Outline each Plasmodium ovale-infected red blood cell.
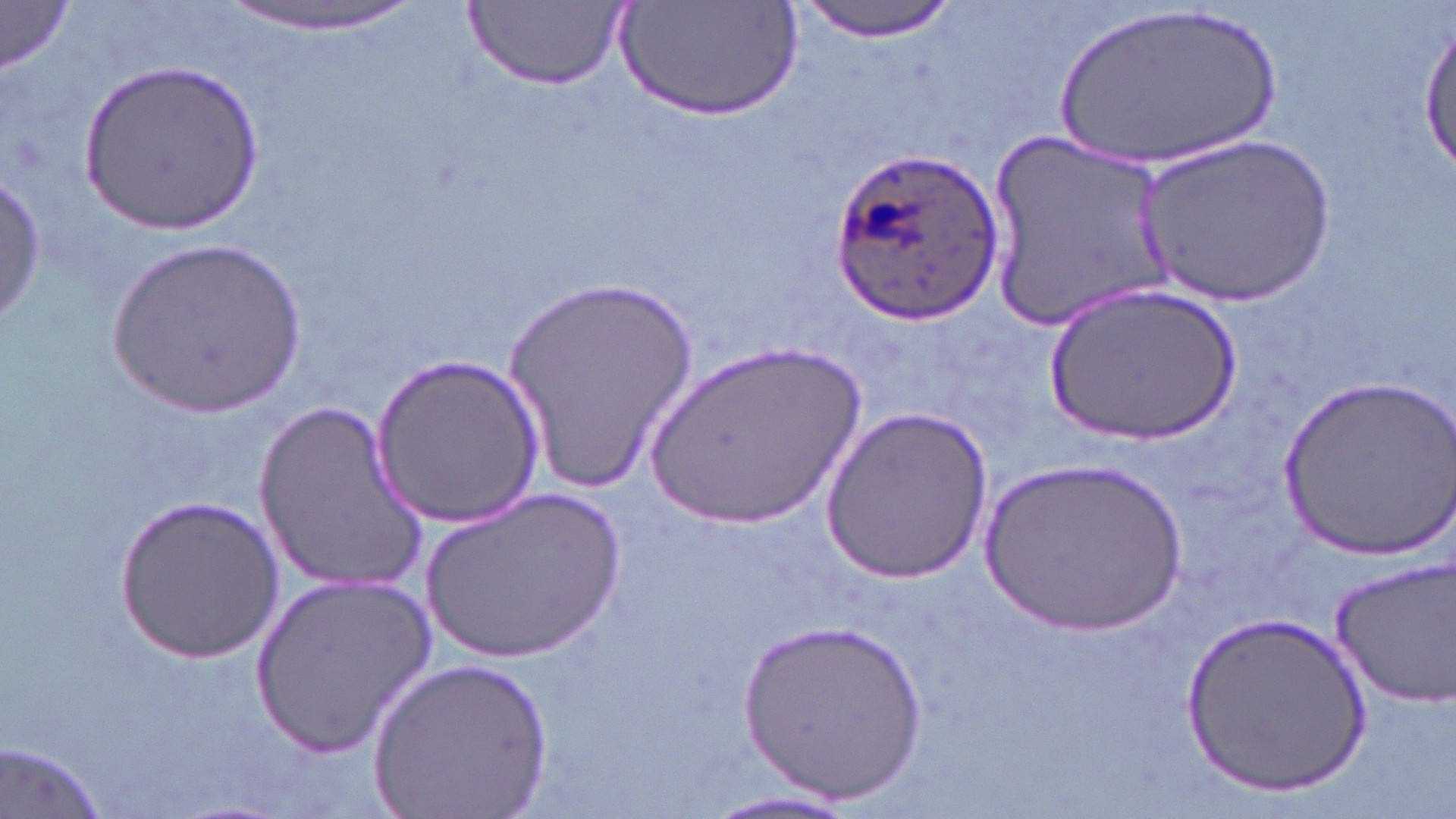

Approximate bounding boxes as (x1, y1, x2, y2) in pixels.
Plasmodium ovale-infected red blood cells: (830, 146, 999, 325).

{
  "slide_level_diagnosis": "Plasmodium ovale",
  "uninfected_red_blood_cell_locations": "approximate bounding boxes as (x1, y1, x2, y2) in pixels: (219, 0, 428, 37), (465, 0, 627, 91), (791, 0, 965, 42), (613, 2, 807, 122), (1048, 2, 1286, 175), (0, 3, 74, 76), (1416, 18, 1454, 182), (81, 59, 266, 234), (985, 132, 1174, 329), (1139, 132, 1335, 309), (1, 168, 45, 332), (106, 238, 308, 424), (501, 280, 699, 497), (1050, 280, 1240, 448), (639, 337, 874, 533), (372, 353, 546, 530), (1282, 375, 1455, 558), (252, 399, 422, 598), (820, 404, 993, 583), (978, 454, 1188, 637), (420, 487, 628, 666), (116, 495, 284, 663), (1327, 554, 1456, 712), (250, 572, 435, 753), (1177, 608, 1374, 796), (740, 621, 930, 801), (369, 656, 552, 819), (1, 738, 111, 819), (685, 784, 873, 819)",
  "modality": "optical microscopy",
  "preparation": "thin blood smear",
  "magnification": "1000x",
  "field_of_view": "single",
  "stain": "May-Grünwald-Giemsa",
  "image_size": "1456×819 pixels"
}